State the blood parasite species.
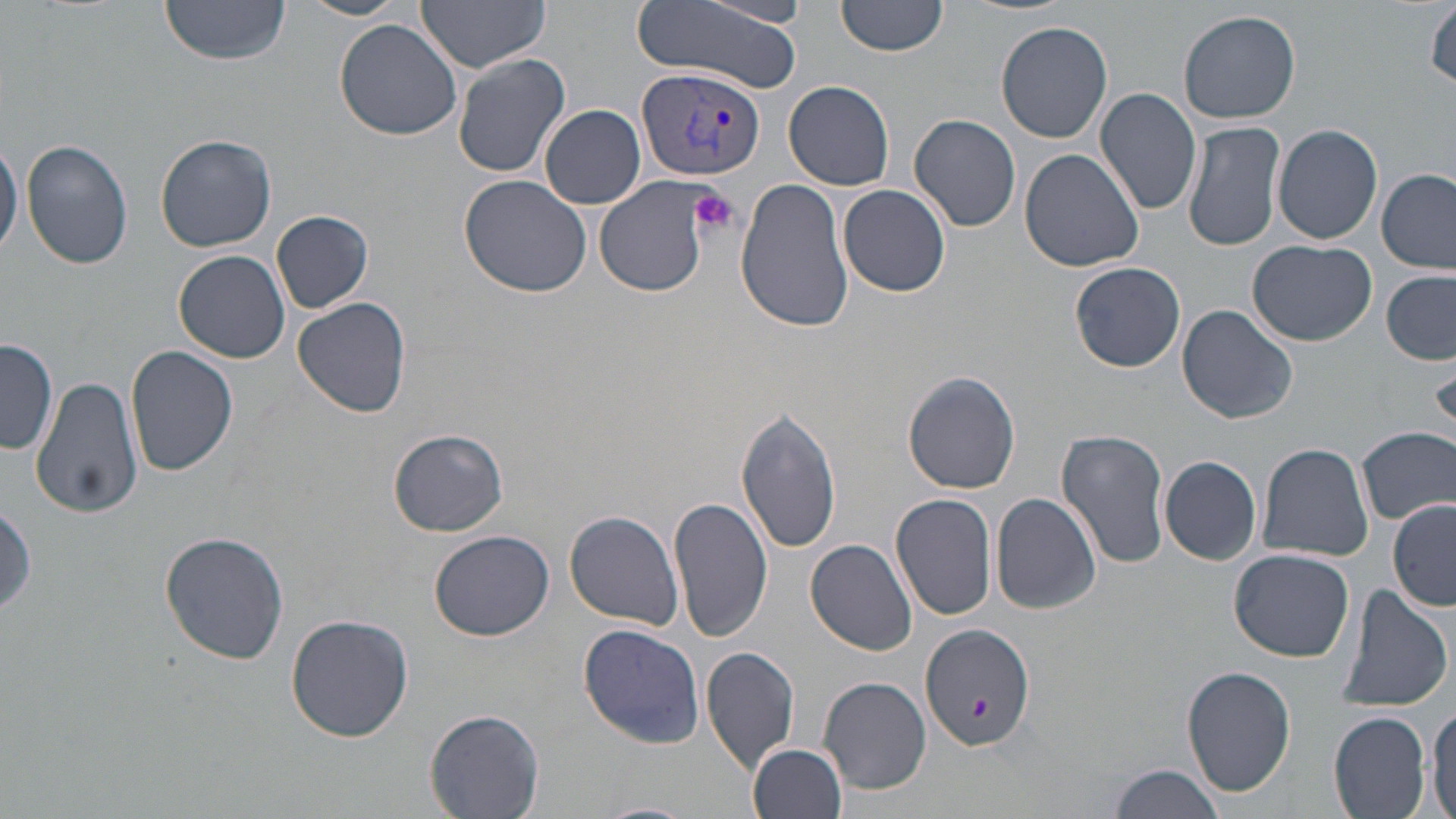
Plasmodium vivax.

Summary:
  - Coordinate format: approximate bounding boxes as (x1, y1, x2, y2) in pixels
  - Plasmodium vivax-infected red blood cell locations: (637, 66, 766, 180)
  - Uninfected red blood cell locations: (160, 0, 292, 65), (298, 0, 410, 22), (415, 0, 552, 72), (631, 0, 804, 91), (837, 0, 947, 57), (701, 2, 816, 28), (1427, 2, 1456, 90), (1178, 9, 1301, 125), (334, 19, 462, 141), (997, 22, 1114, 143), (452, 54, 570, 178), (784, 80, 895, 190), (1095, 87, 1202, 216), (540, 104, 646, 209), (910, 113, 1021, 232), (1182, 119, 1285, 254), (1273, 123, 1385, 246), (156, 133, 278, 252), (0, 134, 22, 262), (21, 138, 135, 270), (1020, 150, 1145, 274), (1377, 168, 1455, 273), (459, 173, 592, 296), (595, 177, 712, 297), (736, 178, 855, 334), (838, 184, 952, 296), (272, 211, 373, 314), (1247, 239, 1377, 346), (172, 248, 291, 364), (1070, 261, 1187, 372), (1382, 271, 1456, 364), (293, 296, 411, 420), (1177, 304, 1298, 424), (1, 339, 59, 456), (126, 346, 237, 477), (903, 371, 1022, 495), (33, 376, 143, 519), (737, 408, 842, 555), (1357, 426, 1456, 526), (387, 428, 509, 536), (1056, 428, 1171, 568), (1258, 442, 1374, 562), (1159, 455, 1262, 564), (891, 491, 997, 621), (991, 493, 1101, 615), (670, 496, 773, 642), (1389, 499, 1455, 612), (0, 500, 38, 621), (564, 511, 684, 629), (429, 530, 555, 641), (159, 531, 290, 665), (807, 539, 918, 655), (1229, 548, 1355, 660), (1332, 583, 1455, 715), (287, 613, 414, 742), (918, 622, 1034, 753), (578, 623, 706, 749), (703, 646, 800, 770), (1181, 665, 1298, 797), (819, 677, 930, 793), (1428, 700, 1456, 819), (425, 708, 544, 818), (1329, 712, 1431, 818), (750, 741, 850, 819), (1108, 763, 1230, 819), (590, 801, 697, 819)
  - Platelet locations: (688, 188, 740, 239), (972, 694, 993, 723)
  - Modality: optical microscopy
  - Image size: 1456×819 pixels
  - Preparation: thin blood film
  - Magnification: 1000x
  - Field of view: single
  - Stain: May-Grünwald-Giemsa